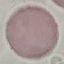
Summary:
  - Malaria status: uninfected
  - Preparation: thin smear
  - Stain: Giemsa
  - Image type: cell patch, automatically extracted from a larger field of view and resized to 64 × 64 pixels
  - Capture: smartphone camera at the microscope eyepiece